Classify this cell by malaria status.
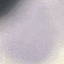

It is uninfected.

image_type: cell patch, automatically extracted from a larger field of view and resized to 64 × 64 pixels
capture: smartphone camera at the microscope eyepiece
stain: Giemsa
preparation: thin smear